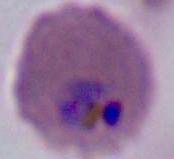
400x or 1000x magnification. A Plasmodium parasite is seen. Photomicrograph.